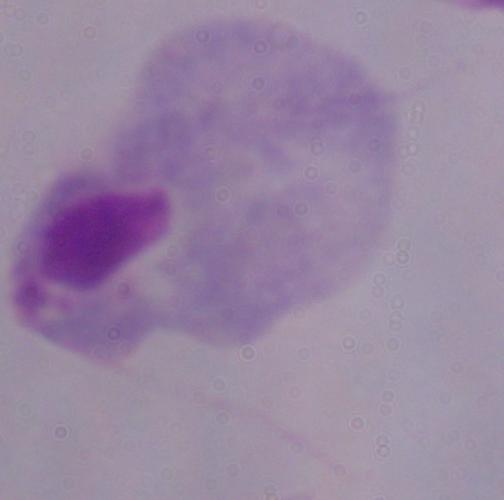
Summary:
  - Modality: photomicrograph
  - Identification: trichomonad
  - Magnification: 1000x